Give the extent of all uninfected red blood cells.
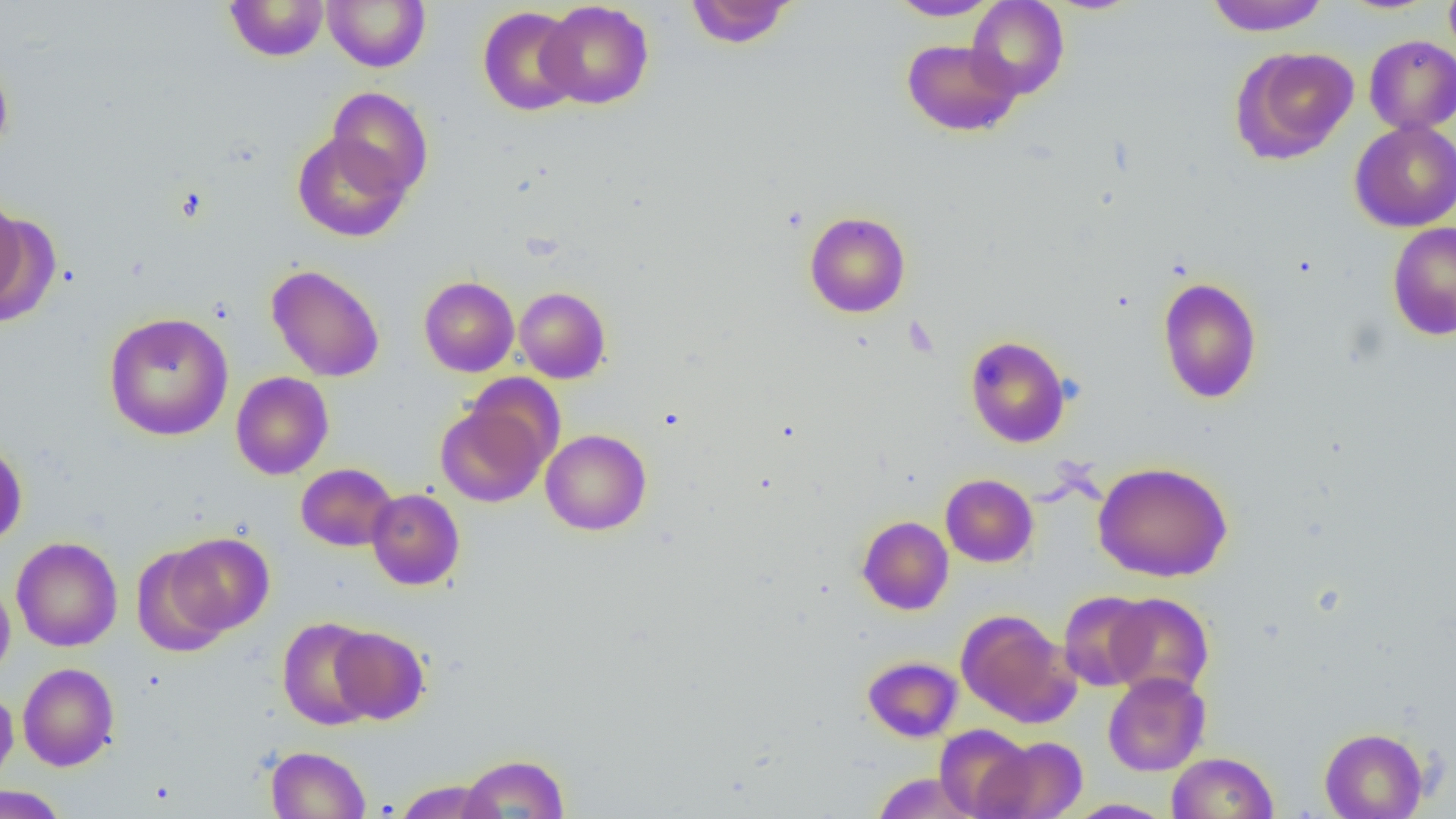

Approximate bounding boxes as (x1, y1, x2, y2) in pixels.
Uninfected red blood cells: (323, 0, 430, 72), (685, 0, 796, 48), (888, 0, 1001, 20), (967, 0, 1069, 99), (1205, 0, 1330, 36), (1444, 0, 1456, 61), (224, 1, 329, 61), (539, 1, 653, 109), (477, 6, 582, 116), (1364, 35, 1456, 135), (901, 39, 1022, 137), (1233, 46, 1359, 163), (0, 56, 14, 158), (326, 86, 434, 200), (1350, 120, 1456, 231), (292, 131, 411, 242), (0, 194, 27, 314), (804, 211, 910, 318), (1387, 222, 1456, 341), (266, 264, 384, 382), (419, 276, 519, 376), (1157, 276, 1262, 404), (514, 286, 611, 384), (103, 312, 234, 441), (965, 335, 1070, 447), (231, 372, 334, 479), (436, 401, 550, 508), (541, 429, 651, 536), (0, 440, 28, 547), (1093, 461, 1233, 582), (296, 463, 398, 551), (940, 474, 1038, 567), (367, 489, 465, 590), (857, 516, 954, 615), (164, 532, 275, 636), (11, 537, 122, 652), (131, 545, 234, 657), (0, 578, 15, 680), (1058, 590, 1156, 692), (1105, 593, 1214, 698), (957, 609, 1078, 727), (276, 617, 379, 730), (330, 626, 430, 724), (862, 655, 962, 742), (17, 663, 119, 771), (1103, 671, 1211, 776), (0, 687, 18, 787), (934, 724, 1035, 818), (1319, 727, 1429, 819), (978, 734, 1088, 819), (265, 745, 370, 818), (1167, 752, 1278, 818), (459, 753, 569, 818), (870, 772, 980, 818), (392, 779, 503, 819), (0, 785, 67, 819), (1063, 799, 1174, 818).

Slide-level diagnosis: no evidence of blood parasites. Image is 1456×819 pixels. Thin blood smear. Optical microscopy. One field of a larger specimen. 1000x magnification.